Point out each Plasmodium parasite.
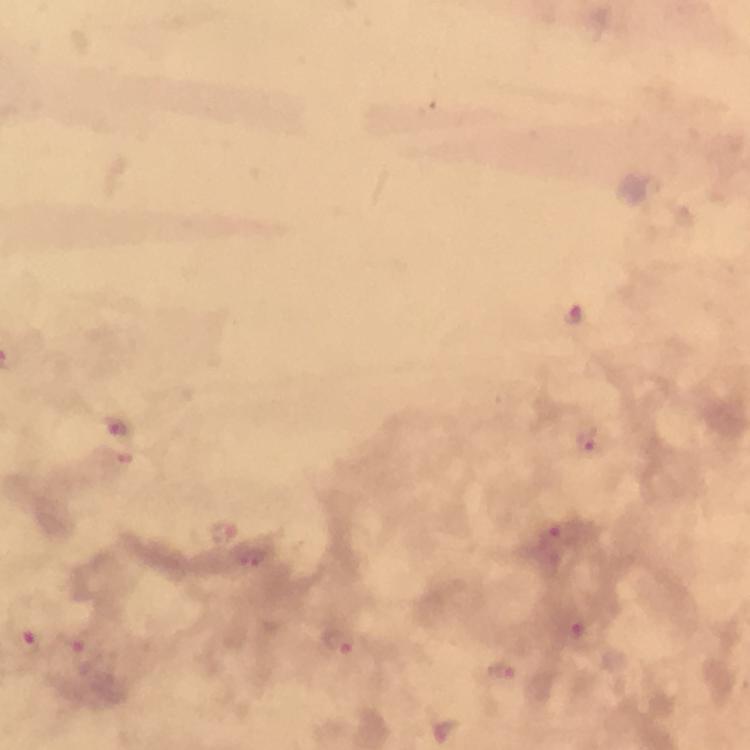

Approximate object centers, in pixels from the top-left corner.
Plasmodium parasites: (x=573, y=316), (x=116, y=427), (x=588, y=443), (x=224, y=531), (x=564, y=533), (x=255, y=558), (x=588, y=635), (x=338, y=638), (x=28, y=641), (x=86, y=658), (x=500, y=671).

image size = 750×750 pixels
cropped from = a single field of view
stain = Giemsa
capture = smartphone mounted on the microscope
immersion oil = applied
magnification = 100x
context = from a diagnostic examination for malaria
preparation = thick blood film